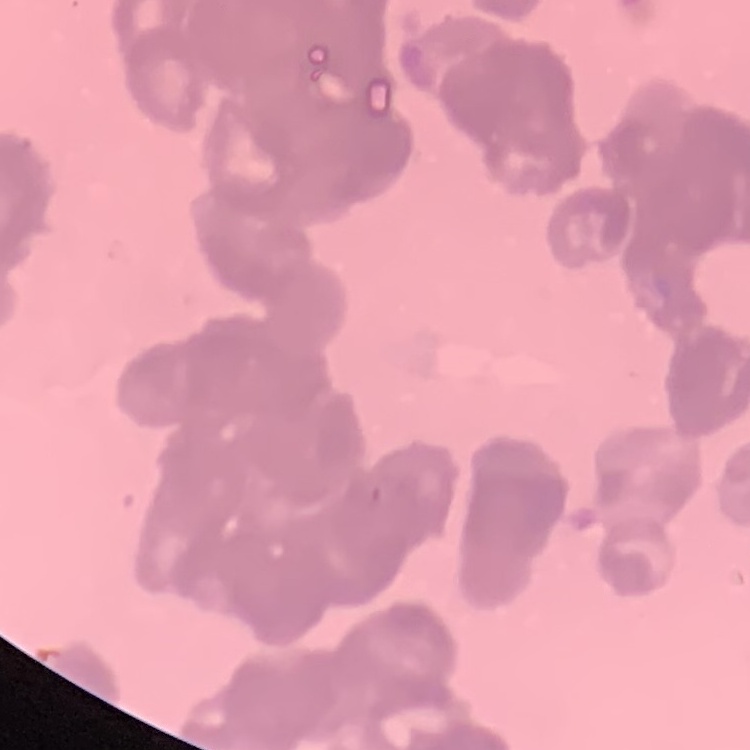
{
  "erythrocyte_morphology": "rouleaux formation",
  "image_type": "one tile cut from a larger photomicrograph",
  "stain": "Field's or Giemsa",
  "preparation": "thin blood smear"
}